Assess the morphology of the erythrocytes.
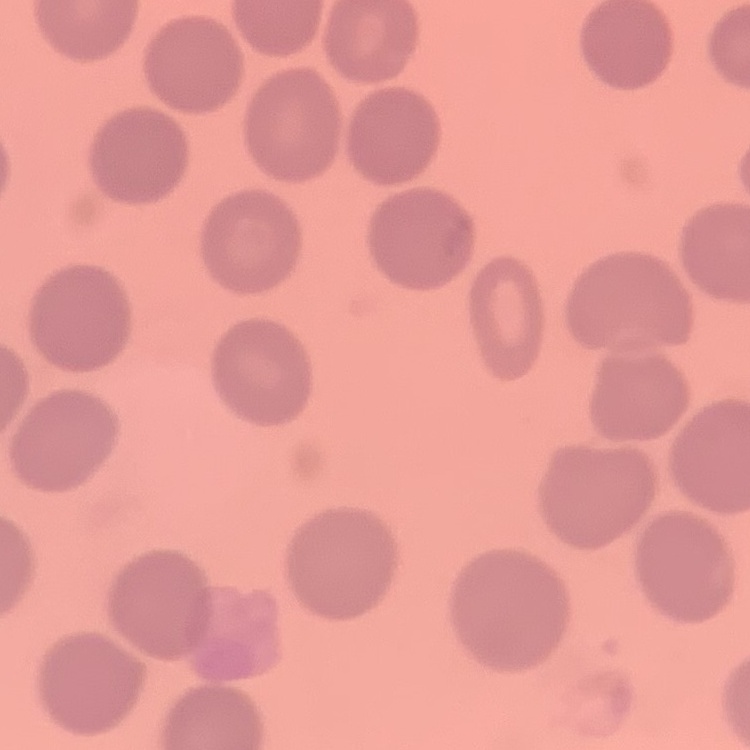

They show no rouleaux formation.

Stained with either Field's or Giemsa. One tile cut from a larger photomicrograph. Thin blood smear.